Locate every Plasmodium falciparum-infected red blood cell.
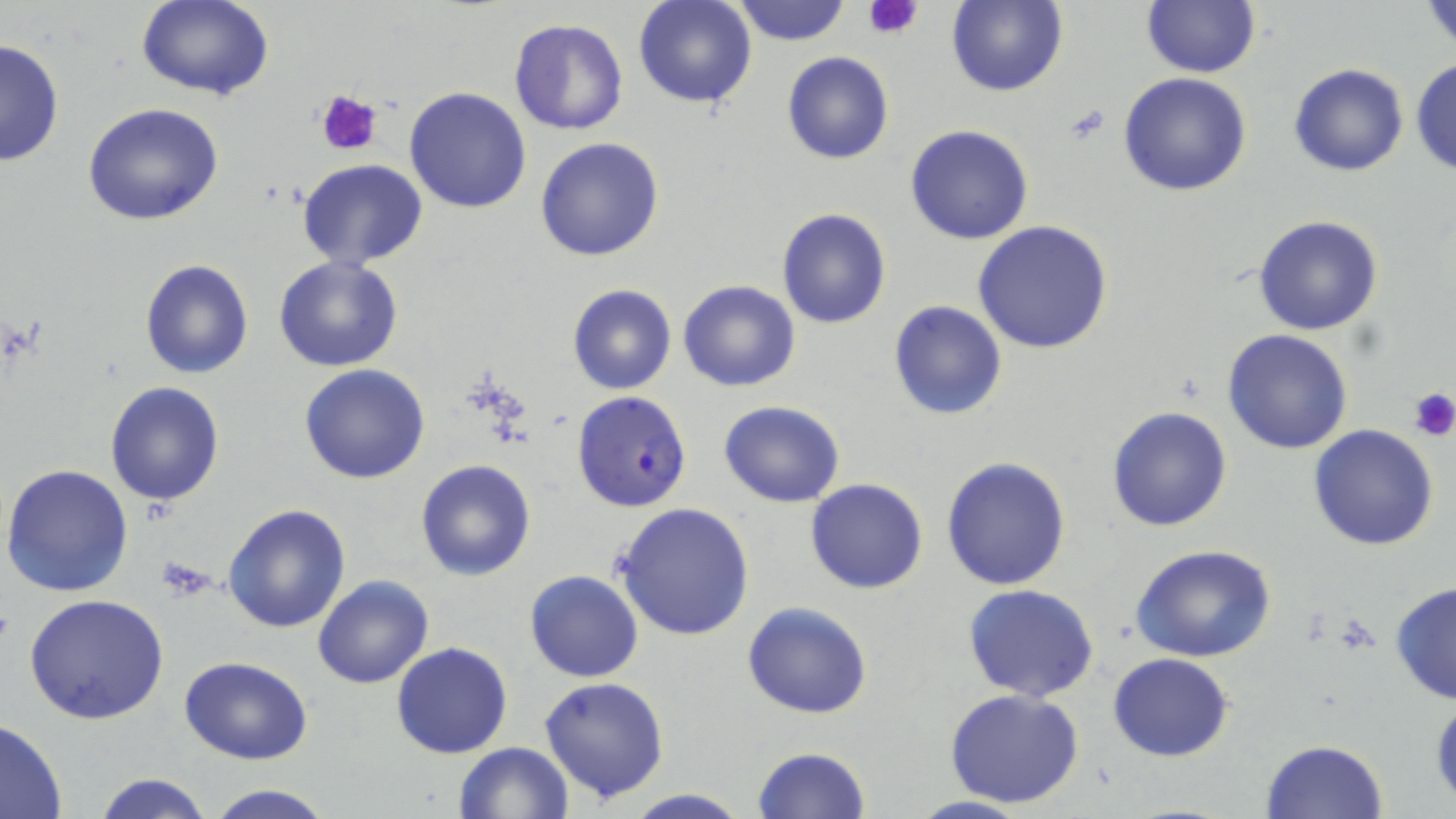

Approximate bounding boxes as [x1, y1, x2, y2] in pixels.
Plasmodium falciparum-infected red blood cells: [572, 391, 692, 512].

Uninfected red blood cell locations: [135, 0, 275, 100], [633, 0, 759, 109], [730, 1, 853, 47], [945, 1, 1068, 97], [1141, 1, 1259, 77], [1422, 1, 1456, 55], [508, 18, 628, 136], [0, 38, 65, 168], [782, 51, 894, 164], [1411, 56, 1456, 180], [1287, 62, 1409, 177], [1118, 72, 1253, 197], [405, 87, 531, 213], [82, 102, 226, 226], [905, 124, 1035, 244], [535, 136, 666, 261], [296, 160, 431, 270], [776, 207, 892, 329], [1253, 214, 1383, 336], [973, 222, 1113, 354], [273, 257, 404, 372], [138, 258, 255, 379], [677, 280, 801, 392], [568, 284, 676, 396], [889, 300, 1007, 420], [1223, 329, 1353, 455], [299, 364, 431, 483], [103, 381, 225, 506], [719, 400, 846, 508], [1107, 406, 1233, 532], [1308, 424, 1439, 552], [940, 457, 1070, 591], [415, 458, 537, 580], [1, 463, 134, 598], [805, 478, 929, 594], [613, 501, 755, 640], [222, 503, 351, 633], [1131, 545, 1278, 663], [524, 569, 643, 683], [313, 575, 435, 691], [1388, 580, 1456, 706], [963, 584, 1099, 700], [24, 594, 170, 723], [742, 602, 873, 719], [391, 641, 513, 758], [1107, 652, 1235, 763], [179, 656, 313, 764], [539, 676, 670, 804], [944, 689, 1086, 809], [1429, 689, 1455, 809], [0, 720, 68, 818], [1261, 740, 1387, 819], [453, 741, 575, 818], [753, 745, 870, 818], [95, 773, 213, 819], [201, 782, 339, 819], [619, 789, 753, 819], [904, 794, 1037, 819]. Platelet locations: [861, 0, 925, 37], [316, 90, 384, 157], [1409, 387, 1455, 443], [158, 557, 216, 600]. Slide-level diagnosis: Plasmodium falciparum. Optical microscopy. May-Grünwald-Giemsa-stained preparation. Image is 1456×819 pixels. Thin blood film. 1000x magnification. Single field of view.